Point out each leukocyte.
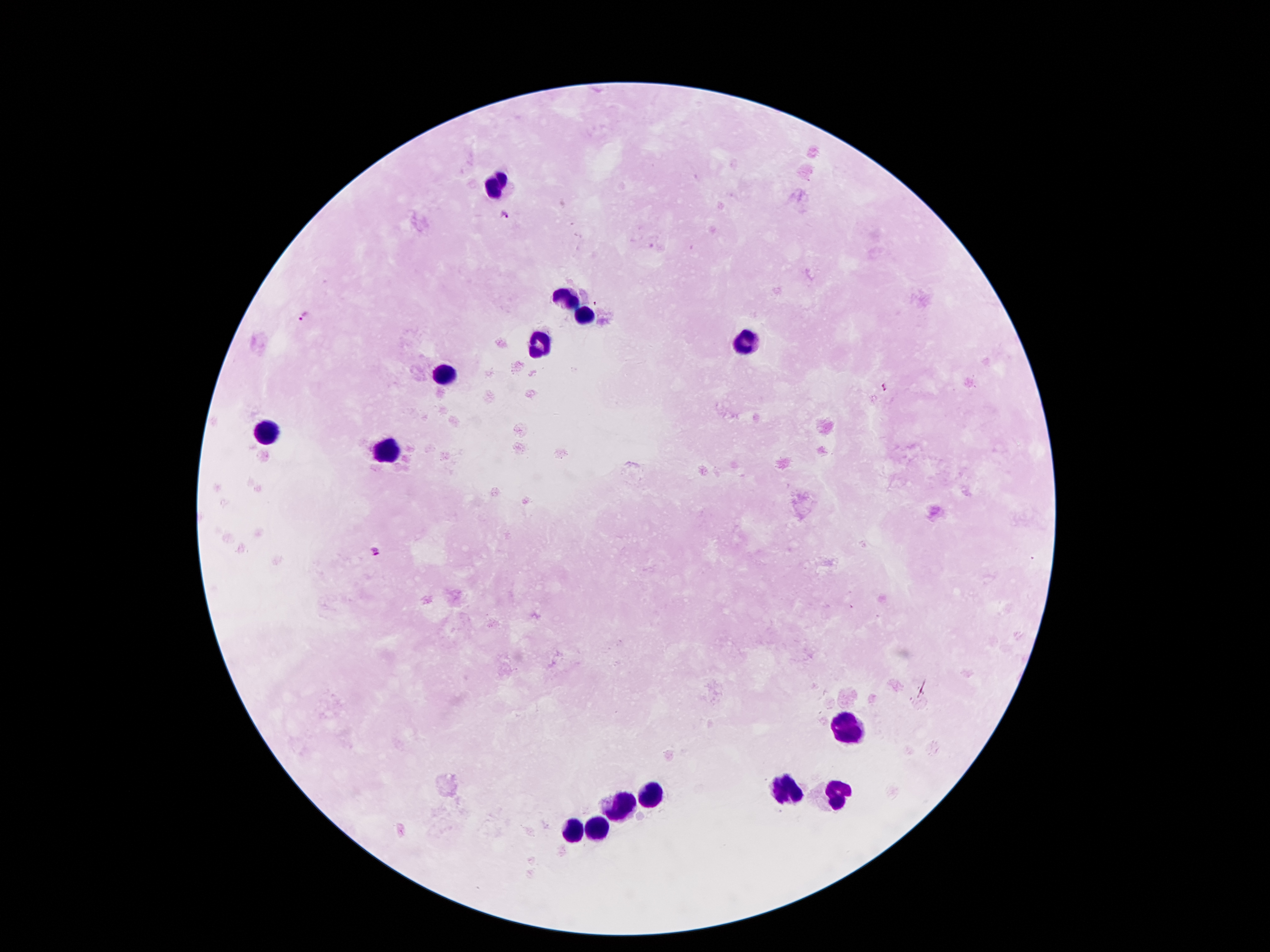
Approximate centers as [x, y] in pixels.
Leukocytes: [496, 185], [567, 300], [583, 318], [744, 343], [544, 347], [446, 374], [265, 433], [385, 448], [848, 728], [789, 788], [839, 793], [651, 794], [621, 804], [597, 829], [574, 832].

{
  "capture": "smartphone through the microscope eyepiece",
  "stain": "Giemsa",
  "patient_malaria_status": "positive for Plasmodium falciparum",
  "plasmodium_parasite_locations": "approximate centers as [x, y] in pixels: [504, 217], [306, 316], [885, 387], [377, 551]",
  "image_size": "1270×952 pixels",
  "magnification": "100x",
  "field_of_view": "single",
  "preparation": "thick blood smear"
}